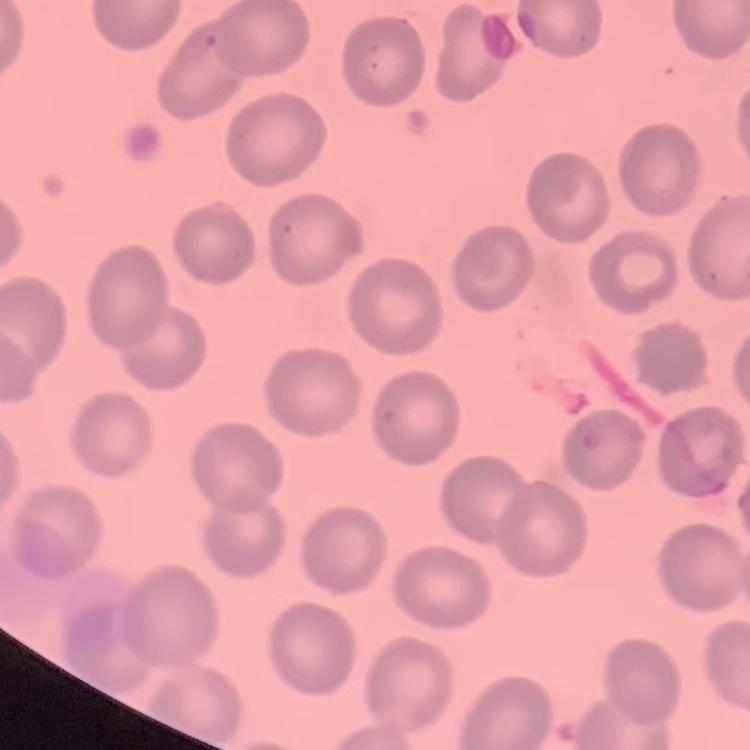

Summary:
  - Erythrocyte morphology: no rouleaux formation
  - Stain: Field's or Giemsa
  - Image type: one tile cut from a larger photomicrograph
  - Preparation: thin blood smear